Evaluate for parasitized red blood cells.
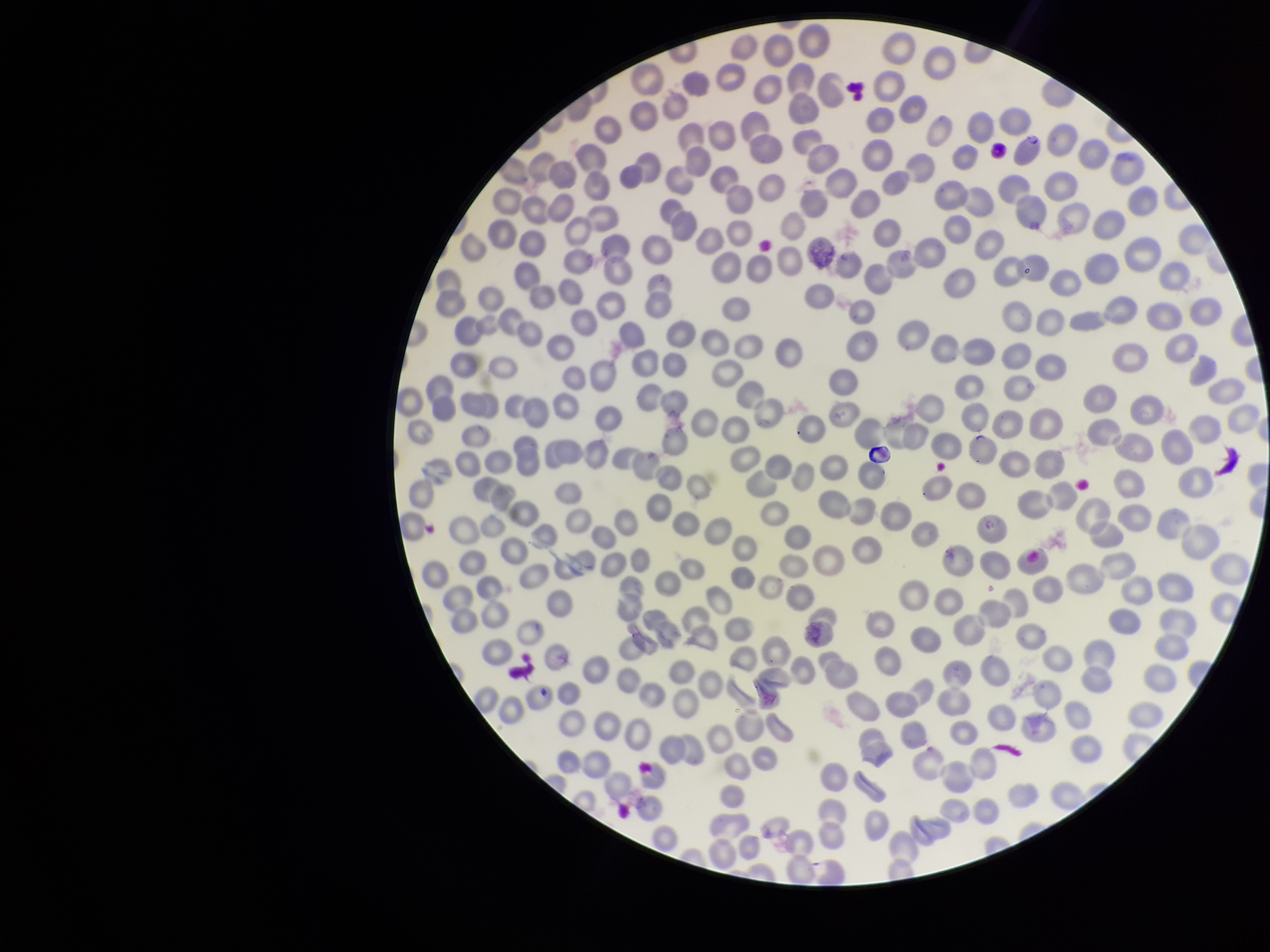

None detected.

Patient malaria status: infected. Parasitized red blood cell count: 0. Giemsa stain. One field from this slide. Image is 1270×952 pixels. Species reported for this patient: Plasmodium falciparum. Preparation: thin blood smear. Red blood cell count: 327. Smartphone photograph taken through the eyepiece of a microscope.